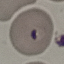

Summary:
  - Result: malaria parasites identified
  - Stain: Giemsa
  - Image type: cell patch, automatically extracted from a larger field of view and resized to 64 × 64 pixels
  - Capture: smartphone camera at the microscope eyepiece
  - Preparation: thin smear